State which parasite is depicted.
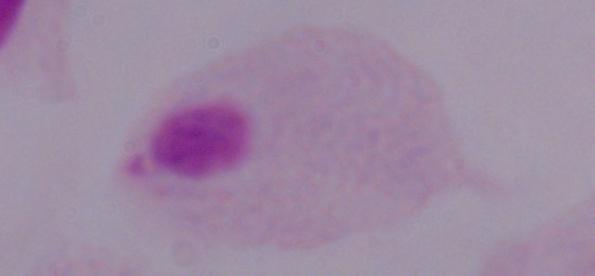
A trichomonad.

1000x magnification. Micrograph.